Report the malaria status of this cell.
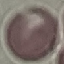
Uninfected.

Automatically extracted cell patch, resized to 64 × 64 pixels. Giemsa stain. Acquired by smartphone through the microscope eyepiece. Thin blood smear.